State which parasite is depicted.
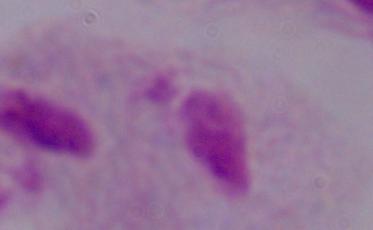

A trichomonad.

Summary:
  - Modality: micrograph
  - Magnification: 1000x